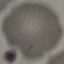

Summary:
  - Malaria status: uninfected
  - Capture: smartphone through the microscope eyepiece
  - Preparation: thin blood film
  - Stain: Giemsa
  - Image type: cell patch, automatically extracted from a larger field of view and resized to 64 × 64 pixels